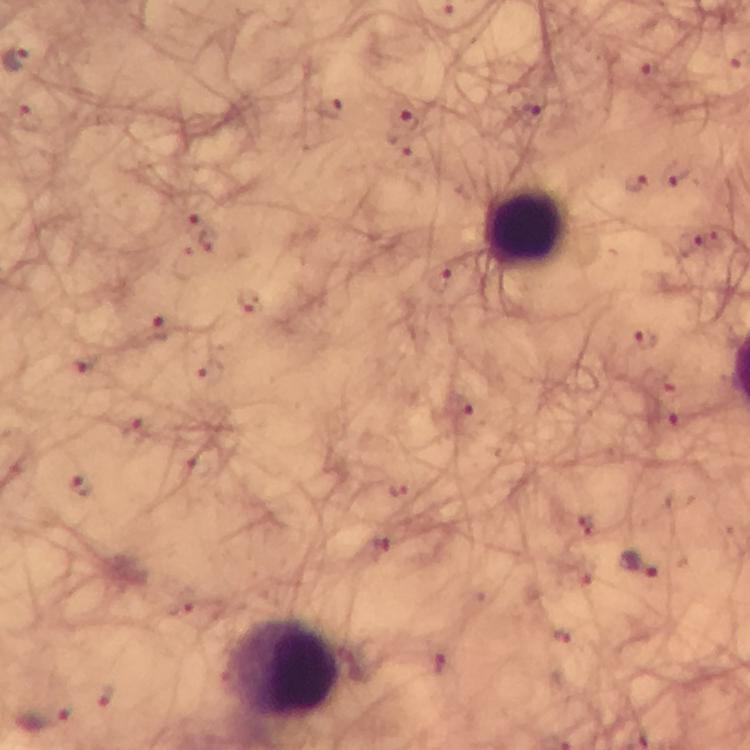
Approximate object centers, in pixels from the top-left corner. Leukocyte locations: (x=523, y=228), (x=283, y=669). Malaria parasite locations: (x=404, y=119), (x=635, y=182), (x=247, y=302), (x=643, y=341), (x=82, y=487), (x=641, y=566), (x=47, y=718). From a diagnostic examination for malaria. Giemsa stain. Photographed with a smartphone mounted on the microscope. Thick blood smear. Image is 750×750 pixels. Immersion oil applied. A crop from one field of view. At 100x magnification.